Report the malaria status of this cell.
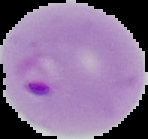
It is parasitized.

Summary:
  - Image type: segmented cell region with the area outside set to black
  - Preparation: thin blood film
  - Image size: 148×139 pixels